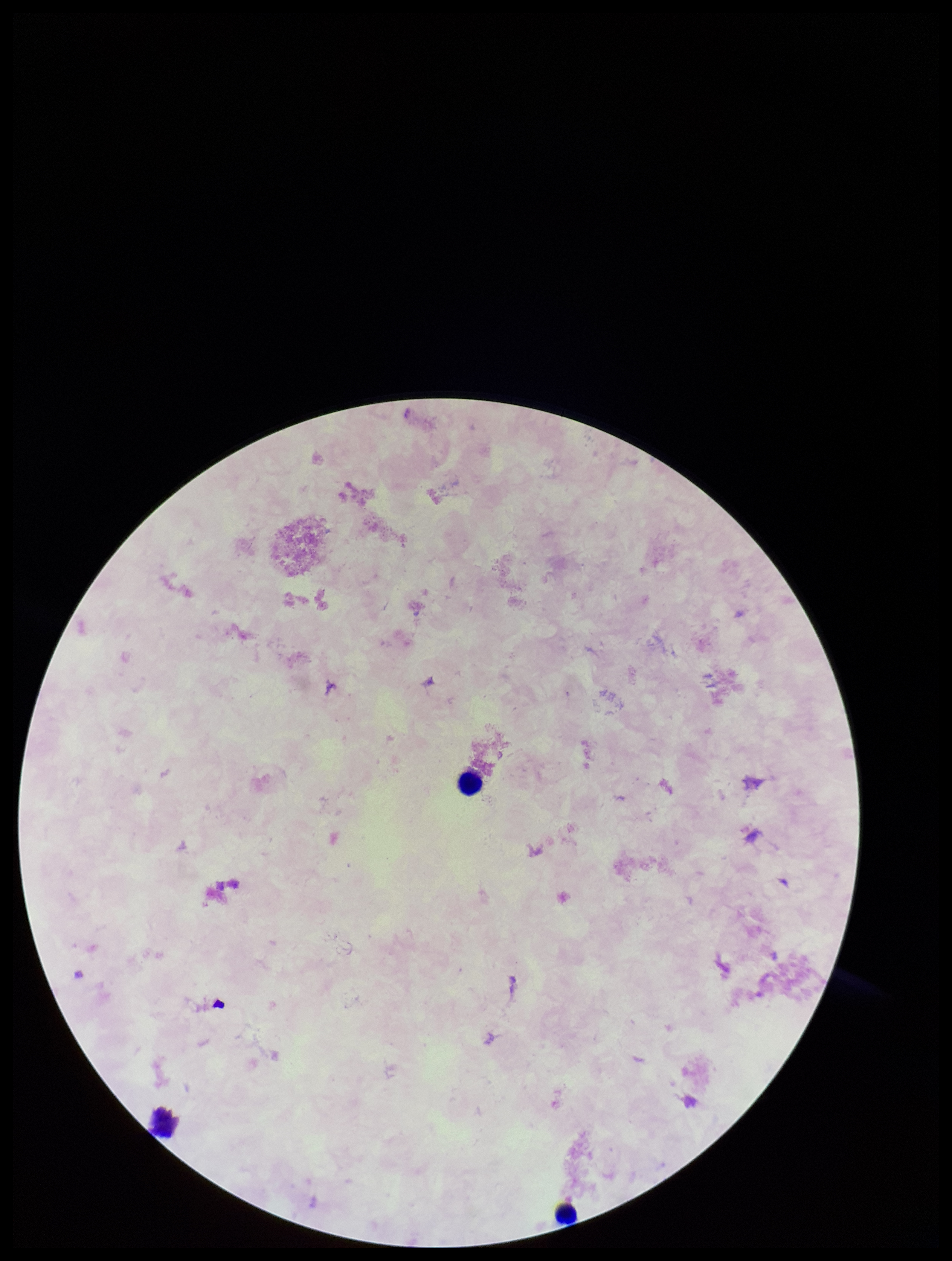

preparation = thick blood smear
capture = smartphone photograph through the microscope eyepiece
image size = 952×1261 pixels
stain = Giemsa
leukocyte count = 3
parasite count = 0
Plasmodium parasites = none identified
field of view = single
patient malaria status = negative